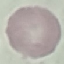
result = negative for malaria parasites
preparation = thin blood smear
image type = automatically extracted cell patch, resized to 64 × 64 pixels
capture = smartphone through the microscope eyepiece
stain = Giemsa